Comment on the morphology of the erythrocytes.
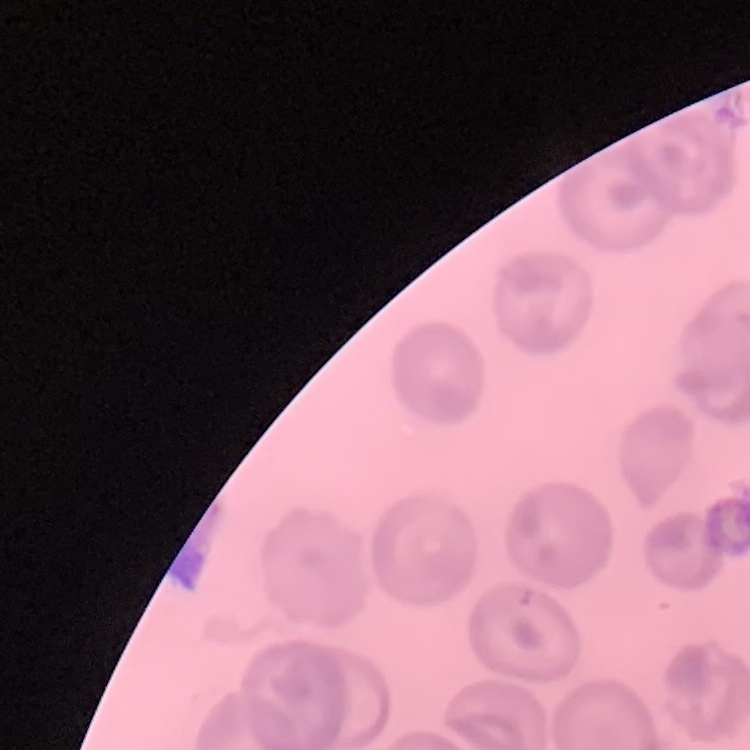
No rouleaux formation.

Thin peripheral smear. Square crop of a larger photomicrograph. Stained with either Field's or Giemsa.